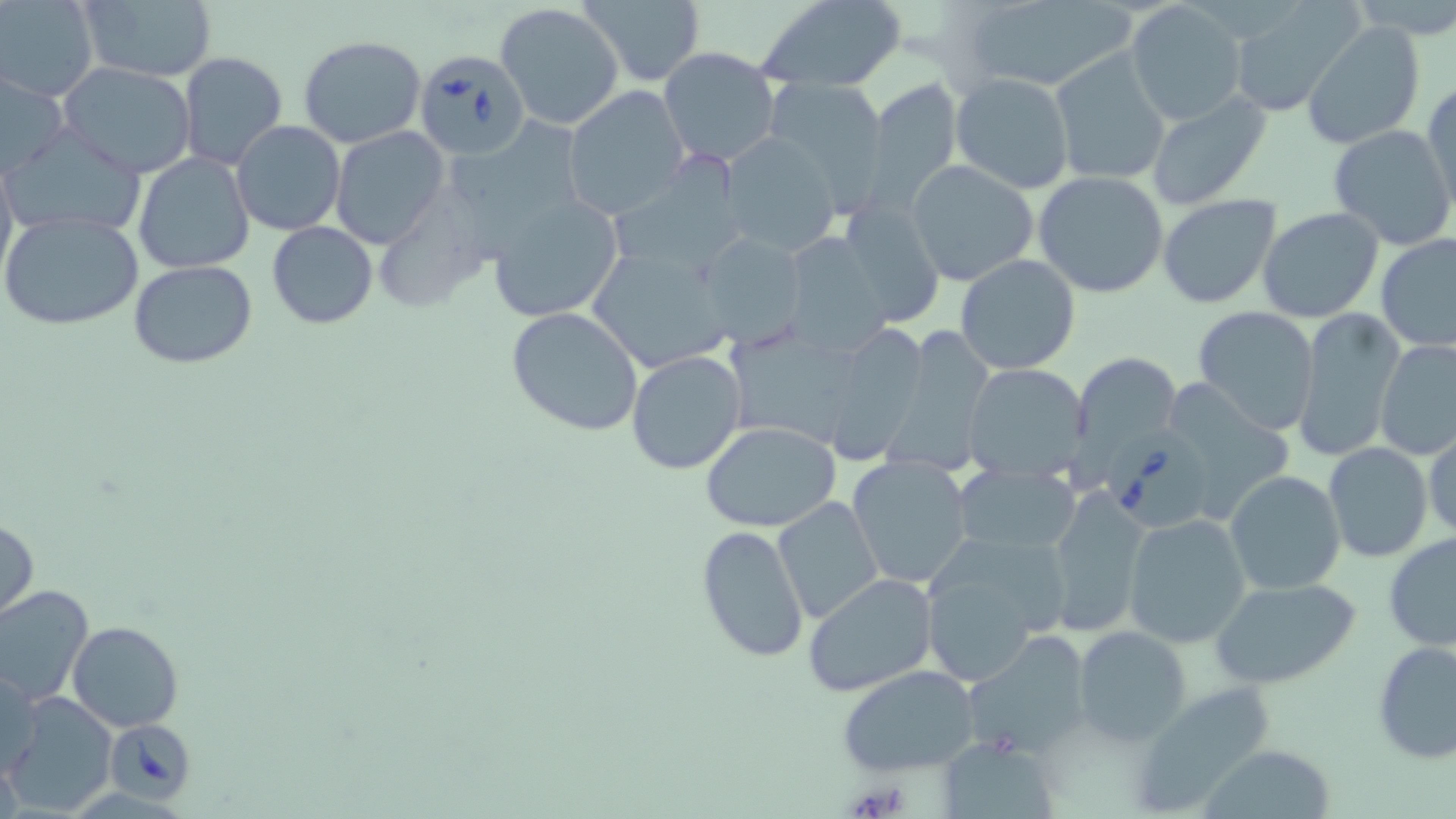

Approximate bounding boxes as named x1/y1/x2/y2 corners in pixels. Uninfected red blood cell locations: (x1=1, y1=0, x2=97, y2=102), (x1=74, y1=0, x2=218, y2=84), (x1=579, y1=0, x2=706, y2=85), (x1=757, y1=0, x2=907, y2=93), (x1=963, y1=0, x2=1133, y2=92), (x1=1344, y1=0, x2=1456, y2=37), (x1=1124, y1=2, x2=1245, y2=126), (x1=496, y1=3, x2=624, y2=129), (x1=1227, y1=4, x2=1361, y2=118), (x1=1303, y1=20, x2=1425, y2=149), (x1=298, y1=35, x2=427, y2=148), (x1=657, y1=47, x2=781, y2=169), (x1=1048, y1=48, x2=1172, y2=186), (x1=177, y1=52, x2=289, y2=172), (x1=58, y1=62, x2=197, y2=177), (x1=1, y1=70, x2=68, y2=179), (x1=951, y1=72, x2=1074, y2=194), (x1=864, y1=76, x2=964, y2=210), (x1=765, y1=79, x2=887, y2=207), (x1=1423, y1=82, x2=1455, y2=218), (x1=561, y1=86, x2=689, y2=218), (x1=1145, y1=88, x2=1272, y2=209), (x1=452, y1=116, x2=584, y2=264), (x1=231, y1=120, x2=345, y2=236), (x1=5, y1=122, x2=148, y2=237), (x1=1327, y1=122, x2=1456, y2=250), (x1=180, y1=125, x2=311, y2=251), (x1=330, y1=127, x2=449, y2=248), (x1=719, y1=133, x2=843, y2=256), (x1=0, y1=150, x2=16, y2=287), (x1=133, y1=152, x2=255, y2=275), (x1=609, y1=154, x2=750, y2=278), (x1=907, y1=158, x2=1040, y2=286), (x1=1034, y1=171, x2=1169, y2=298), (x1=485, y1=192, x2=625, y2=324), (x1=374, y1=193, x2=492, y2=318), (x1=1157, y1=194, x2=1284, y2=309), (x1=838, y1=197, x2=946, y2=329), (x1=1257, y1=207, x2=1385, y2=324), (x1=0, y1=210, x2=145, y2=331), (x1=266, y1=221, x2=377, y2=329), (x1=694, y1=231, x2=808, y2=345), (x1=779, y1=232, x2=893, y2=354), (x1=1373, y1=233, x2=1456, y2=354), (x1=589, y1=245, x2=738, y2=371), (x1=955, y1=254, x2=1081, y2=375), (x1=129, y1=261, x2=259, y2=367), (x1=1290, y1=304, x2=1405, y2=462), (x1=504, y1=305, x2=645, y2=436), (x1=1192, y1=306, x2=1320, y2=435), (x1=826, y1=322, x2=934, y2=472), (x1=880, y1=324, x2=994, y2=484), (x1=726, y1=325, x2=856, y2=444), (x1=1375, y1=338, x2=1456, y2=461), (x1=625, y1=349, x2=747, y2=475), (x1=1069, y1=353, x2=1184, y2=476), (x1=962, y1=362, x2=1091, y2=479), (x1=699, y1=422, x2=845, y2=531), (x1=1424, y1=426, x2=1456, y2=545), (x1=1323, y1=443, x2=1434, y2=564), (x1=845, y1=455, x2=973, y2=589), (x1=951, y1=463, x2=1082, y2=560), (x1=1223, y1=470, x2=1346, y2=594), (x1=1043, y1=487, x2=1152, y2=637), (x1=773, y1=496, x2=884, y2=623), (x1=1124, y1=514, x2=1253, y2=648), (x1=0, y1=515, x2=39, y2=621), (x1=697, y1=526, x2=811, y2=665), (x1=1383, y1=530, x2=1455, y2=653), (x1=923, y1=538, x2=1071, y2=636), (x1=802, y1=573, x2=938, y2=699), (x1=1209, y1=577, x2=1360, y2=689), (x1=0, y1=584, x2=94, y2=708), (x1=931, y1=585, x2=1032, y2=685), (x1=67, y1=620, x2=183, y2=732), (x1=1074, y1=626, x2=1192, y2=745), (x1=967, y1=631, x2=1094, y2=757), (x1=1373, y1=640, x2=1456, y2=766), (x1=2, y1=665, x2=42, y2=781), (x1=838, y1=666, x2=981, y2=775), (x1=1127, y1=681, x2=1280, y2=814), (x1=6, y1=693, x2=118, y2=818), (x1=940, y1=739, x2=1056, y2=817), (x1=1197, y1=745, x2=1336, y2=818). Babesia divergens-infected red blood cell locations: (x1=414, y1=49, x2=533, y2=161), (x1=1101, y1=425, x2=1209, y2=533), (x1=105, y1=717, x2=195, y2=804). Slide-level diagnosis: Babesia divergens. Captured at 1000x magnification. Optical microscopy. May-Grünwald-Giemsa-stained preparation. Image is 1456×819 pixels. Thin blood smear. Single field of view.